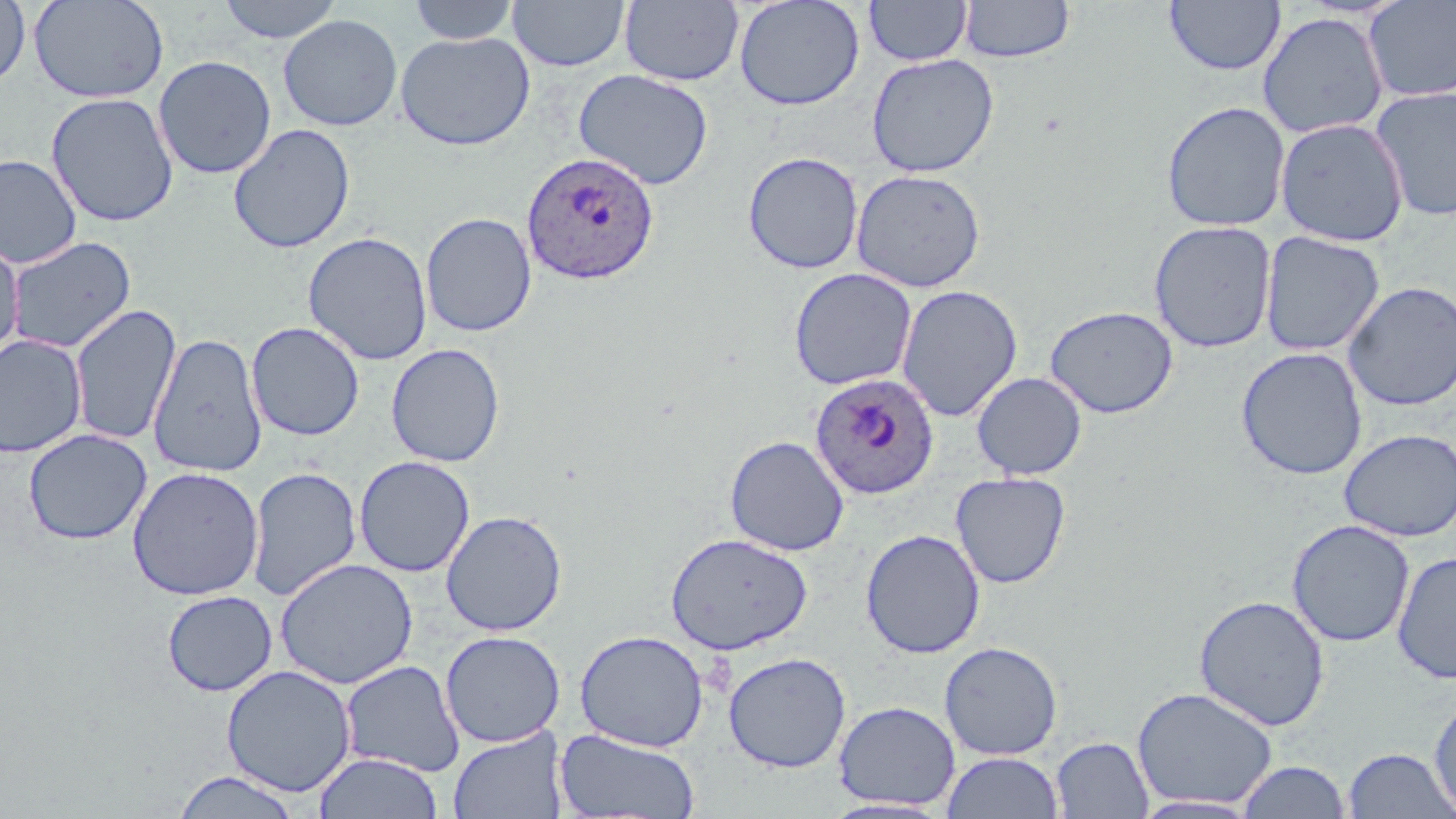

Approximate bounding boxes as named x1/y1/x2/y2 corners in pixels. Uninfected red blood cell locations: (x1=0, y1=0, x2=31, y2=90), (x1=29, y1=0, x2=169, y2=104), (x1=216, y1=0, x2=343, y2=43), (x1=408, y1=0, x2=519, y2=45), (x1=508, y1=0, x2=629, y2=72), (x1=734, y1=0, x2=865, y2=111), (x1=864, y1=0, x2=972, y2=66), (x1=960, y1=0, x2=1075, y2=63), (x1=1362, y1=0, x2=1456, y2=103), (x1=620, y1=1, x2=744, y2=86), (x1=1164, y1=1, x2=1285, y2=77), (x1=1257, y1=12, x2=1389, y2=139), (x1=278, y1=14, x2=403, y2=131), (x1=396, y1=31, x2=535, y2=151), (x1=866, y1=54, x2=999, y2=177), (x1=154, y1=55, x2=276, y2=179), (x1=574, y1=69, x2=714, y2=190), (x1=1370, y1=85, x2=1456, y2=222), (x1=46, y1=92, x2=179, y2=227), (x1=1161, y1=101, x2=1290, y2=232), (x1=1275, y1=118, x2=1409, y2=246), (x1=228, y1=123, x2=356, y2=254), (x1=743, y1=151, x2=865, y2=274), (x1=0, y1=154, x2=82, y2=269), (x1=851, y1=169, x2=987, y2=292), (x1=421, y1=212, x2=537, y2=337), (x1=1148, y1=220, x2=1277, y2=353), (x1=302, y1=231, x2=433, y2=366), (x1=1259, y1=231, x2=1385, y2=358), (x1=0, y1=236, x2=24, y2=360), (x1=5, y1=236, x2=136, y2=355), (x1=788, y1=267, x2=917, y2=390), (x1=1342, y1=280, x2=1456, y2=412), (x1=896, y1=284, x2=1022, y2=422), (x1=69, y1=303, x2=182, y2=446), (x1=1045, y1=305, x2=1178, y2=418), (x1=246, y1=321, x2=365, y2=441), (x1=147, y1=332, x2=268, y2=477), (x1=0, y1=335, x2=87, y2=458), (x1=386, y1=343, x2=506, y2=467), (x1=1236, y1=347, x2=1368, y2=480), (x1=971, y1=372, x2=1087, y2=479), (x1=1339, y1=428, x2=1456, y2=542), (x1=23, y1=429, x2=152, y2=545), (x1=724, y1=435, x2=849, y2=556), (x1=354, y1=455, x2=475, y2=577), (x1=127, y1=466, x2=264, y2=601), (x1=246, y1=466, x2=362, y2=602), (x1=950, y1=471, x2=1071, y2=588), (x1=441, y1=510, x2=567, y2=636), (x1=1287, y1=519, x2=1415, y2=648), (x1=860, y1=529, x2=986, y2=659), (x1=665, y1=532, x2=813, y2=655), (x1=1392, y1=550, x2=1456, y2=685), (x1=275, y1=558, x2=418, y2=689), (x1=162, y1=589, x2=278, y2=696), (x1=1193, y1=594, x2=1330, y2=731), (x1=574, y1=629, x2=709, y2=752), (x1=440, y1=630, x2=565, y2=747), (x1=939, y1=641, x2=1064, y2=760), (x1=723, y1=652, x2=851, y2=773), (x1=340, y1=660, x2=465, y2=777), (x1=221, y1=665, x2=356, y2=797), (x1=1132, y1=686, x2=1279, y2=810), (x1=1428, y1=695, x2=1456, y2=817), (x1=833, y1=701, x2=960, y2=810), (x1=447, y1=726, x2=568, y2=819), (x1=554, y1=728, x2=700, y2=818), (x1=1051, y1=736, x2=1154, y2=818), (x1=1342, y1=747, x2=1454, y2=818), (x1=942, y1=751, x2=1063, y2=818), (x1=313, y1=752, x2=444, y2=818), (x1=1237, y1=760, x2=1352, y2=819), (x1=171, y1=770, x2=303, y2=818), (x1=1131, y1=795, x2=1263, y2=818), (x1=820, y1=797, x2=954, y2=818). Plasmodium ovale-infected red blood cell locations: (x1=521, y1=151, x2=659, y2=285), (x1=809, y1=372, x2=939, y2=500). Slide-level diagnosis: Plasmodium ovale. One field of a larger specimen. Captured at 1000x magnification. Image is 1456×819 pixels. Thin blood film. Light microscopy. May-Grünwald-Giemsa stain.